Assess for Plasmodium parasites.
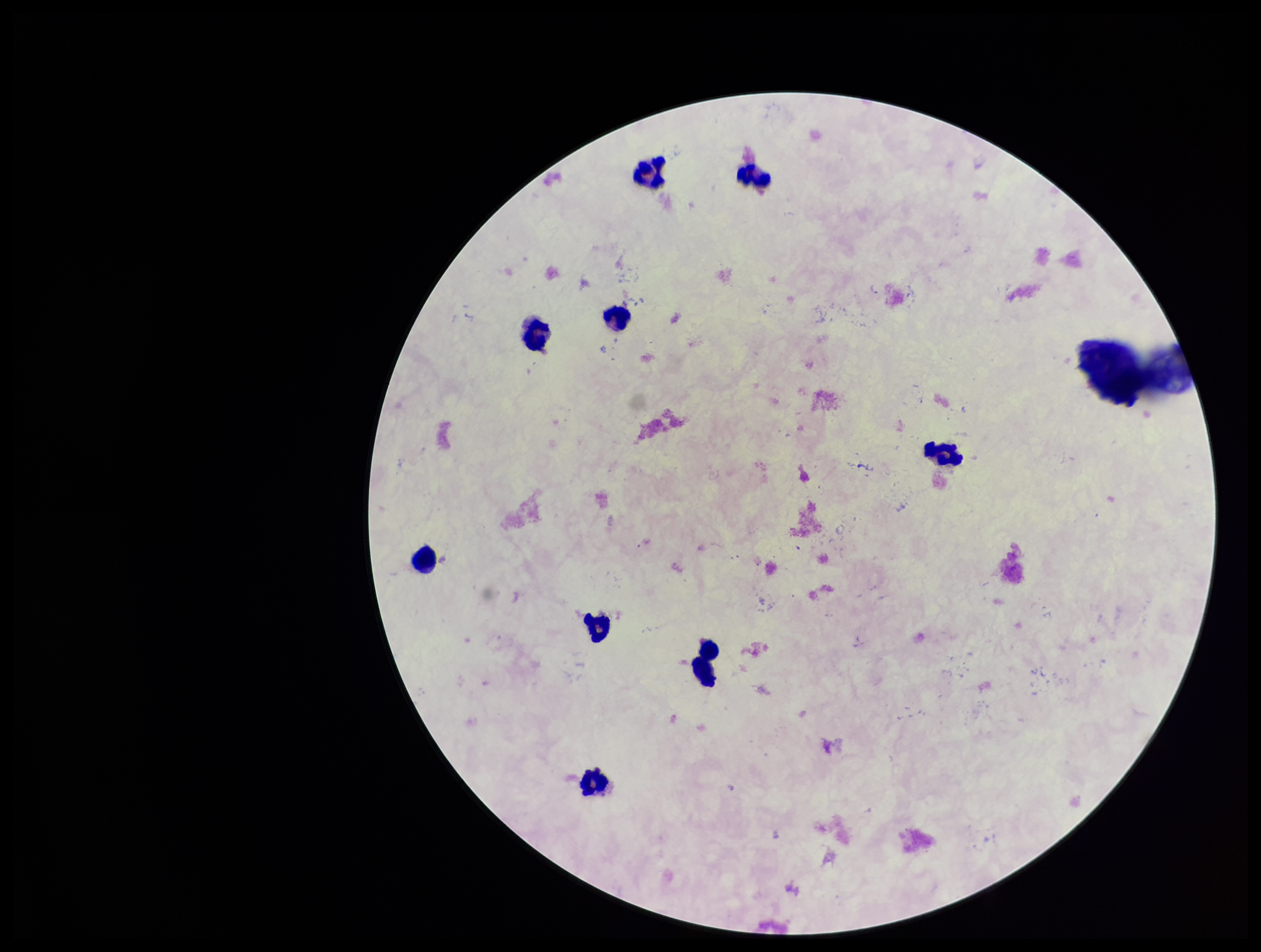
None identified.

Giemsa stain. Patient malaria status: negative. Image is 1261×952 pixels. Photographed through the microscope eyepiece with a smartphone camera. Parasite count: 0. Leukocyte count: 9. One field from this slide. Preparation: thick blood smear.